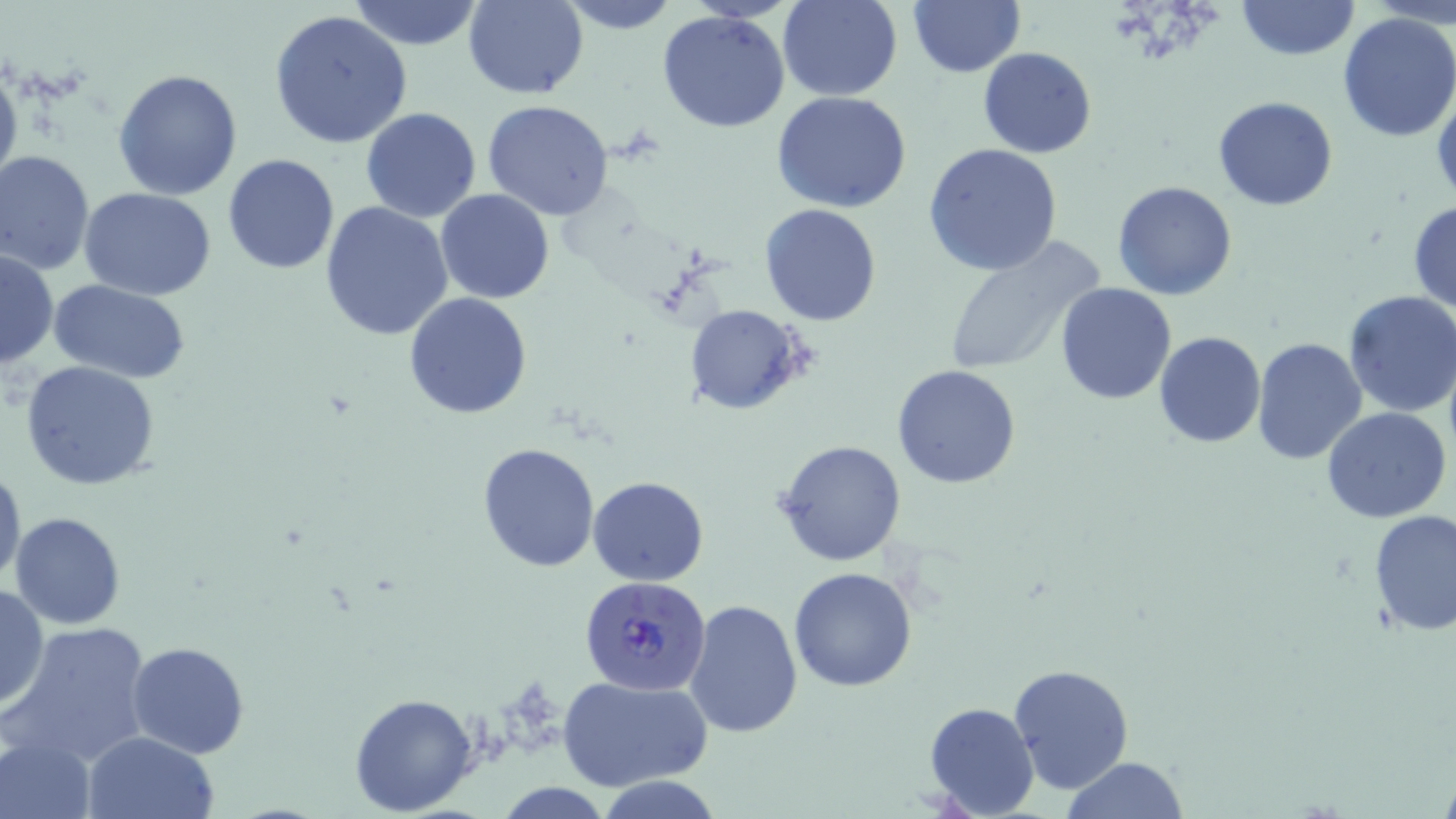
{
  "slide_level_diagnosis": "Plasmodium falciparum",
  "modality": "light microscopy",
  "field_of_view": "one of a larger specimen",
  "stain": "May-Grünwald-Giemsa",
  "image_size": "1456×819 pixels",
  "uninfected_red_blood_cell_locations": "approximate bounding boxes as [x1, y1, x2, y2] in pixels: [348, 0, 483, 50], [777, 0, 904, 102], [908, 0, 1025, 77], [1236, 0, 1359, 61], [463, 1, 588, 99], [557, 1, 680, 34], [269, 8, 413, 150], [657, 10, 791, 133], [1335, 11, 1456, 142], [978, 46, 1097, 159], [0, 53, 22, 200], [111, 68, 243, 201], [772, 90, 914, 213], [1212, 95, 1338, 213], [480, 99, 615, 221], [360, 108, 483, 222], [924, 143, 1064, 275], [1, 149, 98, 275], [223, 154, 341, 274], [1113, 180, 1238, 300], [77, 185, 217, 300], [435, 189, 554, 305], [1407, 199, 1456, 312], [321, 200, 454, 341], [759, 204, 881, 325], [940, 236, 1107, 375], [0, 247, 60, 372], [49, 280, 191, 383], [1055, 281, 1178, 404], [1342, 289, 1456, 418], [403, 293, 532, 420], [687, 306, 806, 414], [1154, 331, 1266, 447], [1251, 336, 1367, 468], [21, 360, 162, 490], [892, 364, 1021, 487], [1322, 407, 1451, 524], [775, 439, 906, 568], [475, 443, 601, 572], [0, 463, 26, 593], [588, 476, 709, 585], [1367, 509, 1456, 635], [11, 512, 125, 628], [788, 566, 917, 691], [0, 584, 50, 711], [685, 599, 803, 738], [5, 620, 154, 768], [126, 641, 250, 757], [1008, 663, 1133, 795], [556, 673, 713, 792], [349, 691, 479, 814], [922, 701, 1039, 818], [84, 731, 220, 819], [1, 734, 98, 818], [1059, 756, 1190, 818], [597, 778, 724, 818]",
  "plasmodium_falciparum_infected_red_blood_cell_locations": "approximate bounding boxes as [x1, y1, x2, y2] in pixels: [579, 575, 713, 694]",
  "preparation": "thin blood film",
  "magnification": "1000x"
}